Outline each blood parasite and name the species.
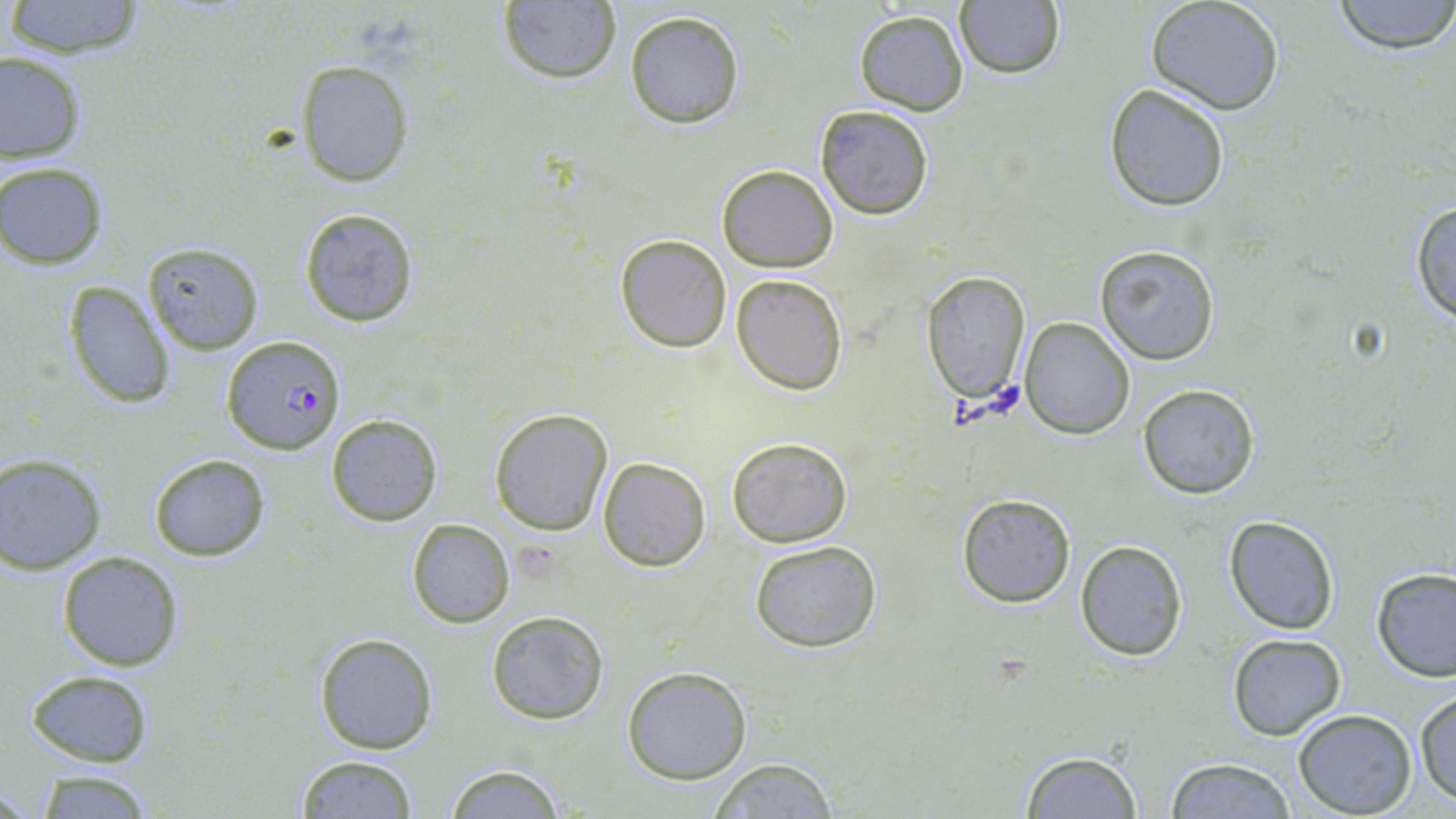
Approximate bounding boxes as named x1/y1/x2/y2 corners in pixels.
Plasmodium falciparum-infected red blood cells: (x1=221, y1=335, x2=347, y2=455).
No Plasmodium ovale, Plasmodium malariae, Plasmodium vivax, Babesia divergens, or Trypanosoma brucei observed.

Summary:
  - Uninfected red blood cell locations: (x1=3, y1=0, x2=148, y2=60), (x1=1329, y1=0, x2=1456, y2=54), (x1=497, y1=2, x2=622, y2=84), (x1=954, y1=2, x2=1067, y2=79), (x1=1147, y1=2, x2=1285, y2=114), (x1=853, y1=9, x2=970, y2=115), (x1=624, y1=10, x2=745, y2=128), (x1=1124, y1=33, x2=1261, y2=176), (x1=0, y1=51, x2=87, y2=163), (x1=297, y1=60, x2=413, y2=185), (x1=1104, y1=83, x2=1230, y2=211), (x1=814, y1=104, x2=933, y2=220), (x1=1, y1=162, x2=108, y2=269), (x1=718, y1=164, x2=837, y2=272), (x1=1410, y1=199, x2=1456, y2=326), (x1=299, y1=206, x2=419, y2=328), (x1=615, y1=235, x2=732, y2=352), (x1=141, y1=242, x2=264, y2=354), (x1=1095, y1=245, x2=1220, y2=365), (x1=921, y1=271, x2=1031, y2=406), (x1=732, y1=273, x2=847, y2=395), (x1=63, y1=281, x2=174, y2=409), (x1=1021, y1=317, x2=1135, y2=437), (x1=1138, y1=383, x2=1259, y2=499), (x1=489, y1=408, x2=613, y2=536), (x1=325, y1=414, x2=444, y2=527), (x1=726, y1=436, x2=852, y2=548), (x1=148, y1=454, x2=269, y2=561), (x1=0, y1=455, x2=106, y2=574), (x1=599, y1=458, x2=711, y2=571), (x1=956, y1=493, x2=1075, y2=607), (x1=1224, y1=516, x2=1338, y2=635), (x1=407, y1=518, x2=515, y2=628), (x1=1076, y1=539, x2=1186, y2=660), (x1=750, y1=541, x2=883, y2=654), (x1=57, y1=550, x2=185, y2=671), (x1=1370, y1=568, x2=1456, y2=682), (x1=485, y1=609, x2=610, y2=725), (x1=315, y1=634, x2=437, y2=754), (x1=1227, y1=635, x2=1345, y2=740), (x1=622, y1=666, x2=751, y2=784), (x1=27, y1=670, x2=154, y2=768), (x1=1414, y1=688, x2=1456, y2=805), (x1=1293, y1=709, x2=1417, y2=817), (x1=1020, y1=749, x2=1142, y2=817), (x1=295, y1=755, x2=423, y2=818), (x1=1164, y1=757, x2=1300, y2=817), (x1=706, y1=758, x2=842, y2=818), (x1=443, y1=765, x2=568, y2=818), (x1=30, y1=770, x2=163, y2=818)
  - Slide-level diagnosis: Plasmodium falciparum
  - Stain: May-Grünwald-Giemsa
  - Preparation: thin blood film
  - Field of view: one of a larger specimen
  - Modality: optical microscopy
  - Image size: 1456×819 pixels
  - Magnification: 1000x